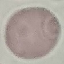

Summary:
  - Result: no malaria parasites detected
  - Preparation: thin blood film
  - Capture: smartphone camera at the microscope eyepiece
  - Image type: cell patch, automatically extracted from a larger field of view and resized to 64 × 64 pixels
  - Stain: Giemsa